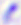
Summary:
  - Magnification: 400x
  - Identification: Toxoplasma gondii
  - Modality: micrograph